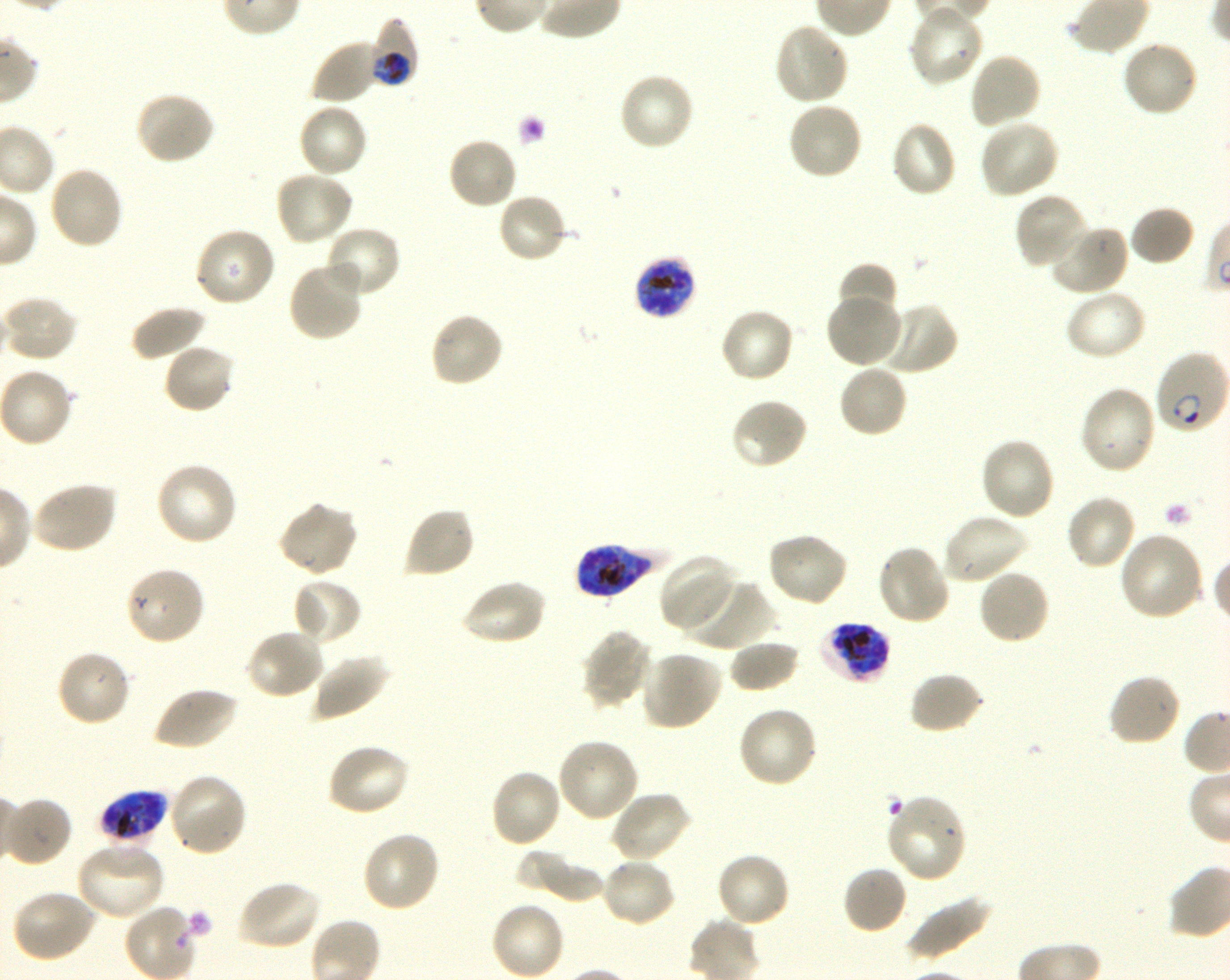
Not every red blood cell is marked. A life-cycle stage — or a range of stages, where the recorded stages span more than one — follows each staged infected red blood cell.
{
  "culture": "Plasmodium falciparum strain 3D7, shaking, in vitro",
  "preparation": "thin blood smear",
  "stain": "Giemsa",
  "locations_of_uninfected_red_blood_cells": "approximate bounding boxes as [x1, y1, x2, y2] in pixels: [908, 4, 985, 88], [772, 22, 849, 106], [310, 38, 380, 106], [1120, 39, 1201, 118], [968, 52, 1042, 130], [618, 72, 695, 152], [135, 91, 216, 165], [786, 101, 864, 182], [296, 102, 368, 179], [977, 118, 1061, 200], [890, 121, 958, 199], [447, 135, 520, 211], [46, 165, 124, 250], [274, 170, 354, 247], [1013, 191, 1088, 270], [496, 193, 570, 264], [1129, 205, 1196, 266], [1049, 222, 1130, 296], [323, 225, 401, 299], [194, 227, 277, 309], [287, 261, 365, 342], [836, 263, 897, 322], [1064, 288, 1147, 362], [824, 294, 903, 369], [2, 296, 79, 363], [876, 302, 958, 375], [130, 304, 206, 362], [719, 307, 796, 384], [428, 310, 505, 388], [163, 342, 236, 414], [837, 363, 908, 439], [0, 367, 75, 448], [1078, 384, 1158, 476], [730, 397, 808, 471], [978, 436, 1056, 522], [154, 462, 240, 548], [29, 481, 118, 554], [1065, 493, 1139, 572], [277, 501, 358, 578], [403, 506, 476, 579], [940, 512, 1028, 584], [766, 531, 850, 608], [1117, 532, 1206, 621], [876, 543, 952, 627], [659, 555, 738, 633], [124, 565, 206, 646], [977, 568, 1051, 646], [291, 577, 363, 646], [460, 578, 547, 646], [684, 578, 774, 651], [244, 628, 326, 701], [581, 629, 653, 709], [728, 638, 800, 693], [55, 650, 132, 728], [640, 650, 724, 731], [311, 654, 390, 721], [909, 671, 985, 735], [1107, 673, 1181, 747], [152, 686, 239, 752], [737, 706, 819, 789], [556, 737, 640, 822], [324, 742, 410, 817], [488, 768, 563, 848], [167, 772, 249, 857], [609, 790, 691, 864], [5, 796, 72, 867], [361, 830, 442, 913], [75, 840, 166, 921], [515, 848, 581, 897], [714, 851, 792, 929], [531, 854, 607, 904], [600, 857, 677, 929], [842, 865, 909, 935], [236, 879, 321, 951], [10, 888, 97, 963], [905, 892, 992, 961], [489, 901, 567, 980]",
  "donor_blood_group": "O+",
  "objective": "100x, oil immersion, numerical aperture 1.30",
  "locations_of_red_blood_cells_of_indeterminate_infection_status": "approximate bounding boxes as [x1, y1, x2, y2] in pixels: [884, 793, 968, 884]",
  "field_of_view": "one from this slide",
  "image_size": "1230×980 pixels",
  "life_cycle_stages_observed": "ring, trophozoite",
  "locations_of_infected_red_blood_cells": "approximate bounding boxes as [x1, y1, x2, y2] in pixels: [366, 18, 418, 89] trophozoite; [634, 255, 696, 320] late trophozoite to late schizont; [1153, 351, 1229, 435] ring; [574, 543, 664, 597] late trophozoite to late schizont; [817, 620, 892, 684] late trophozoite to late schizont; [98, 789, 169, 846] late trophozoite to late schizont"
}